State which parasite is depicted.
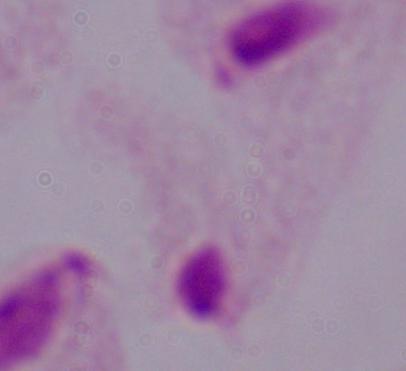

This is a trichomonad.

modality = photomicrograph
magnification = 1000x